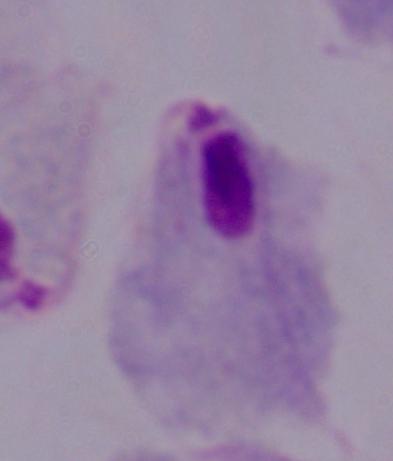

Summary:
  - Identification: trichomonad
  - Modality: photomicrograph
  - Magnification: 1000x